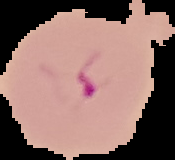
result: malaria parasites identified
image_type: segmented cell region on a black background
preparation: thin blood film
image_size: 175×160 pixels